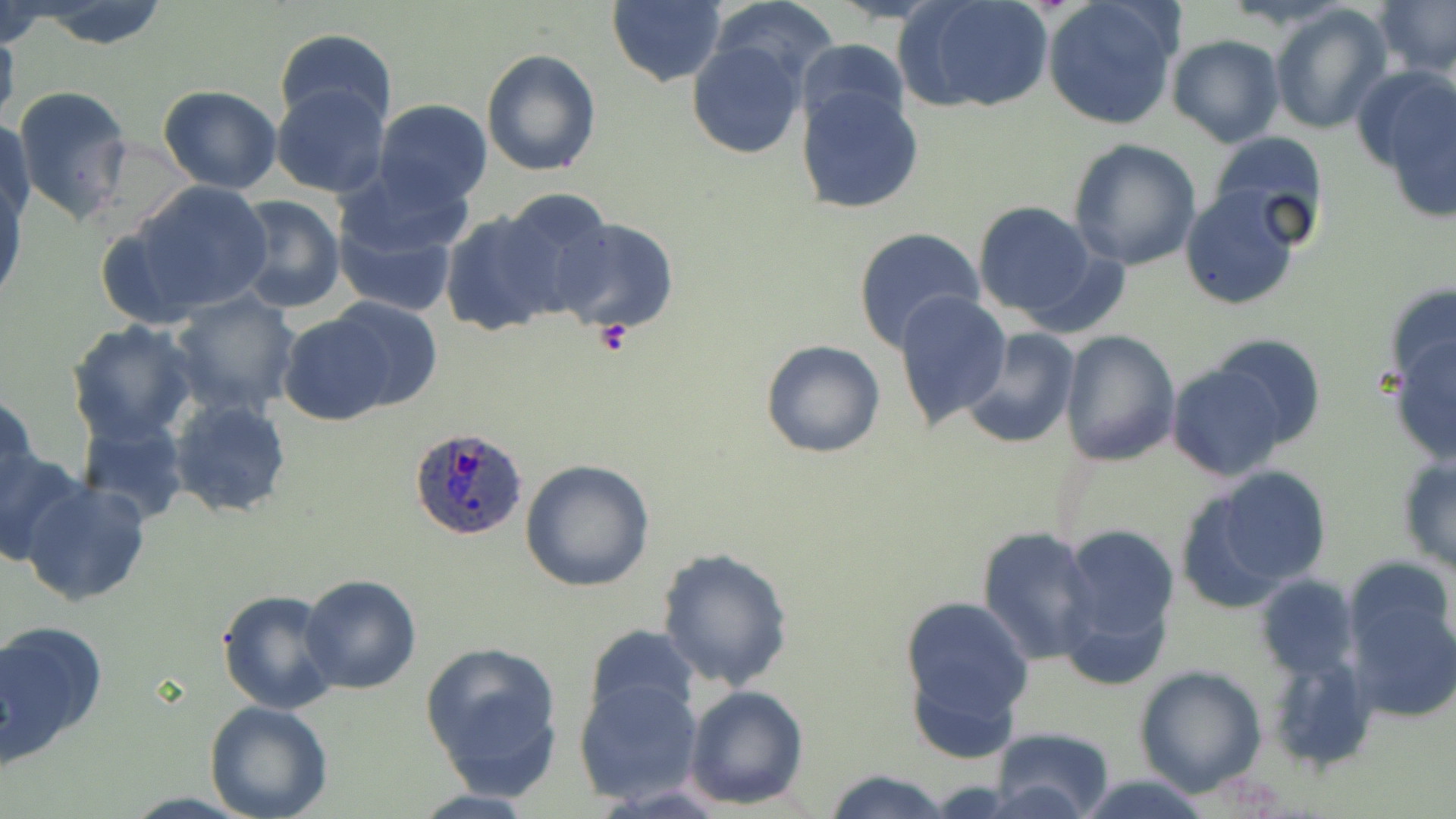

Summary:
  - Coordinate format: approximate bounding boxes as (x1,y1)-(x2,y2) corner pairs in pixels
  - Uninfected red blood cell locations: (26,1)-(176,52), (607,1)-(726,87), (706,1)-(840,93), (901,1)-(1056,114), (1041,1)-(1184,131), (1374,1)-(1456,78), (0,2)-(55,52), (1269,2)-(1393,135), (0,18)-(20,136), (273,28)-(397,130), (1167,35)-(1286,149), (796,36)-(909,135), (686,40)-(808,161), (479,48)-(601,177), (1358,65)-(1456,208), (271,84)-(391,197), (157,85)-(283,195), (797,85)-(924,215), (11,86)-(133,226), (372,100)-(493,209), (1,115)-(36,233), (1203,130)-(1328,249), (1069,139)-(1201,270), (1,175)-(27,307), (122,180)-(276,322), (331,181)-(468,317), (1179,186)-(1304,311), (484,190)-(616,324), (230,194)-(344,315), (972,200)-(1102,324), (437,203)-(574,336), (551,217)-(678,334), (851,226)-(984,354), (895,290)-(1013,430), (170,291)-(302,420), (330,296)-(441,412), (276,310)-(401,426), (67,320)-(201,445), (959,327)-(1080,450), (1388,328)-(1456,465), (1057,329)-(1179,466), (1200,333)-(1326,454), (761,339)-(887,458), (1167,363)-(1294,481), (0,394)-(38,505), (168,398)-(293,519), (77,416)-(189,526), (0,447)-(90,567), (519,458)-(657,592), (1397,458)-(1456,574), (1179,468)-(1336,607), (20,479)-(152,607), (1057,523)-(1180,676), (977,525)-(1099,664), (657,548)-(794,690), (1345,556)-(1456,666), (299,573)-(421,694), (1253,573)-(1360,680), (216,590)-(343,715), (897,593)-(1037,750), (1348,593)-(1456,723), (0,621)-(107,763), (583,625)-(700,725), (419,639)-(565,800), (1263,649)-(1383,774), (1134,666)-(1267,797), (574,678)-(704,806), (685,683)-(811,809), (205,701)-(335,819), (985,728)-(1116,819), (823,770)-(953,819), (1075,774)-(1219,817)
  - Platelet locations: (590,319)-(636,358)
  - Plasmodium ovale-infected red blood cell locations: (410,428)-(532,540)
  - Slide-level diagnosis: Plasmodium ovale
  - Preparation: thin blood film
  - Field of view: single
  - Modality: light microscopy
  - Image size: 1456×819 pixels
  - Magnification: 1000x
  - Stain: May-Grünwald-Giemsa